Classify this cell by malaria status.
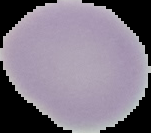

It is uninfected.

Summary:
  - Image size: 151×133 pixels
  - Image type: segmented cell region with the area outside set to black
  - Preparation: thin blood smear